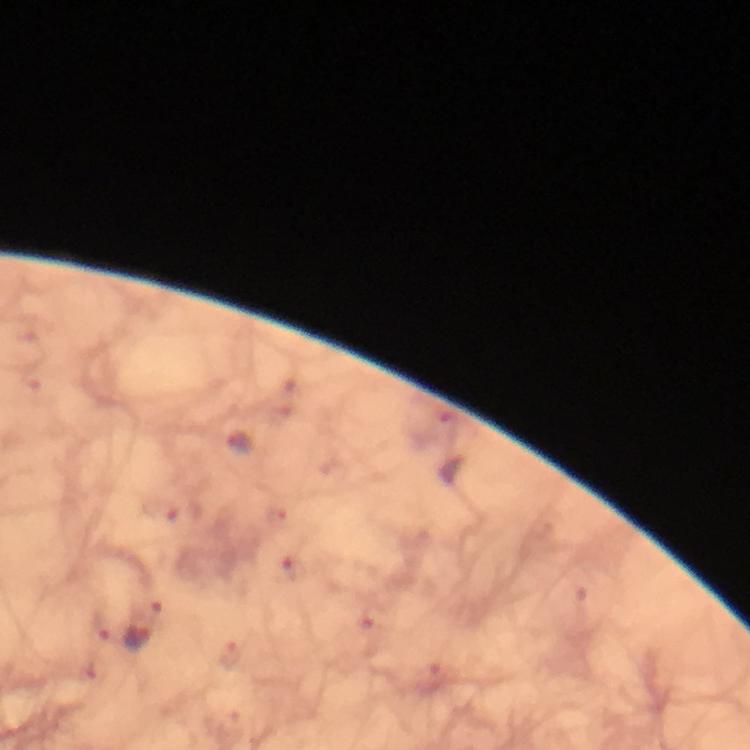
Approximate centers as {x, y} in pixels.
Summary:
  - Plasmodium parasite locations: {137, 638}
  - Cropped from: a single field of view
  - Context: from a malaria diagnostic workup
  - Preparation: thick smear
  - Stain: Giemsa
  - Image size: 750×750 pixels
  - Capture: smartphone mounted on the microscope
  - Immersion oil: used
  - Magnification: 100x